Outline every leukocyte.
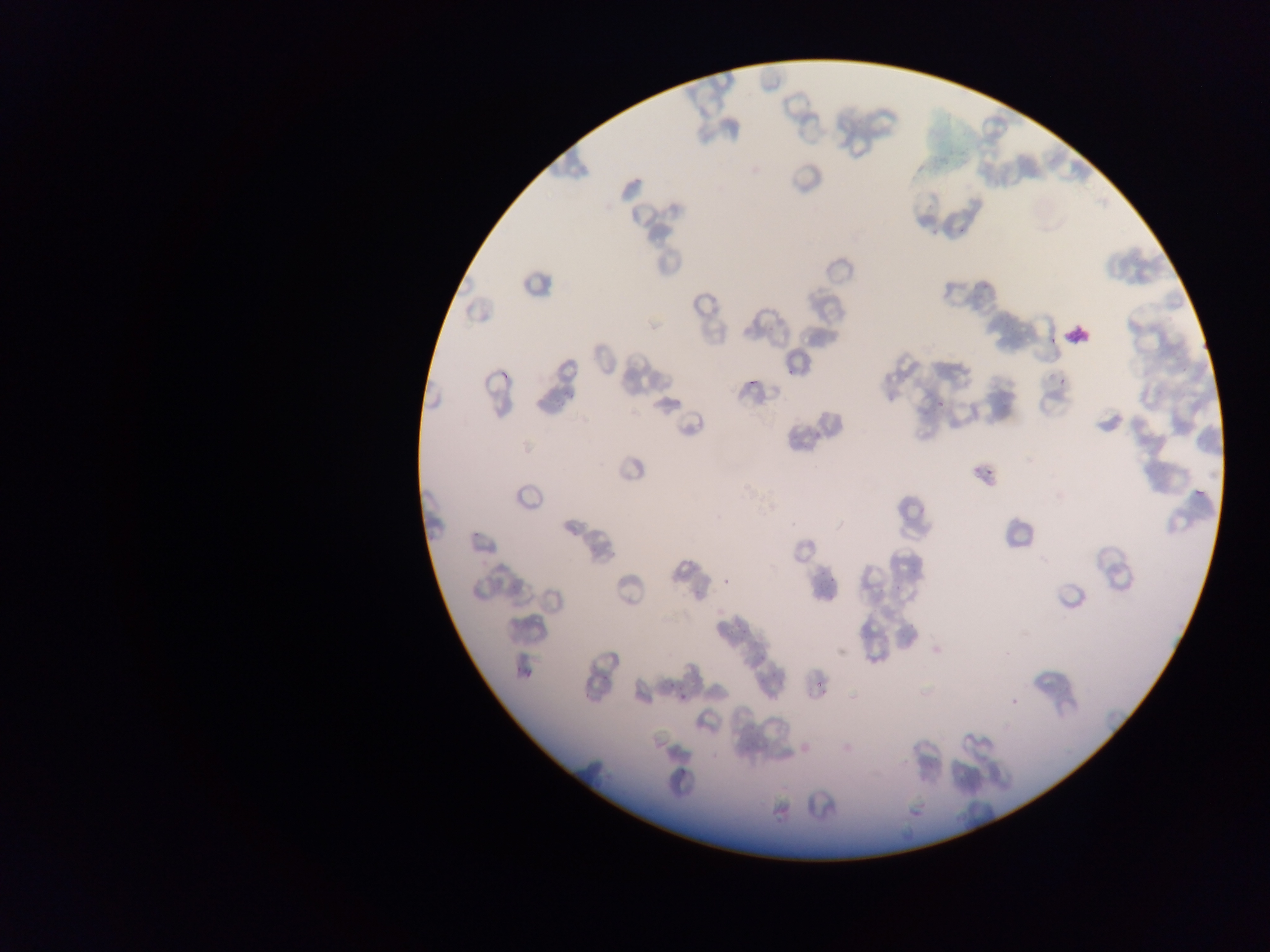

Approximate bounding boxes as {left, top, right, bottom} in pixels.
Leukocytes: {1062, 325, 1088, 345}.

malaria parasite locations = approximate bounding boxes as {left, top, right, bottom} in pixels: {1048, 335, 1059, 345}, {787, 365, 795, 379}, {750, 378, 757, 388}, {1060, 378, 1069, 384}, {934, 393, 947, 413}, {984, 464, 996, 476}, {1193, 489, 1208, 502}, {470, 524, 478, 537}, {721, 575, 732, 585}, {513, 667, 522, 674}, {527, 667, 533, 678}, {668, 680, 674, 689}, {816, 680, 824, 689}, {677, 693, 691, 700}, {680, 768, 690, 779}
field of view = single
image size = 1270×952 pixels
preparation = thin blood film
capture = mobile-phone photograph through a microscope
country = Ghana